Classify this cell by malaria status.
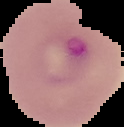

Parasitized.

Summary:
  - Image size: 124×127 pixels
  - Image type: segmented cell region on a black background
  - Preparation: thin blood film